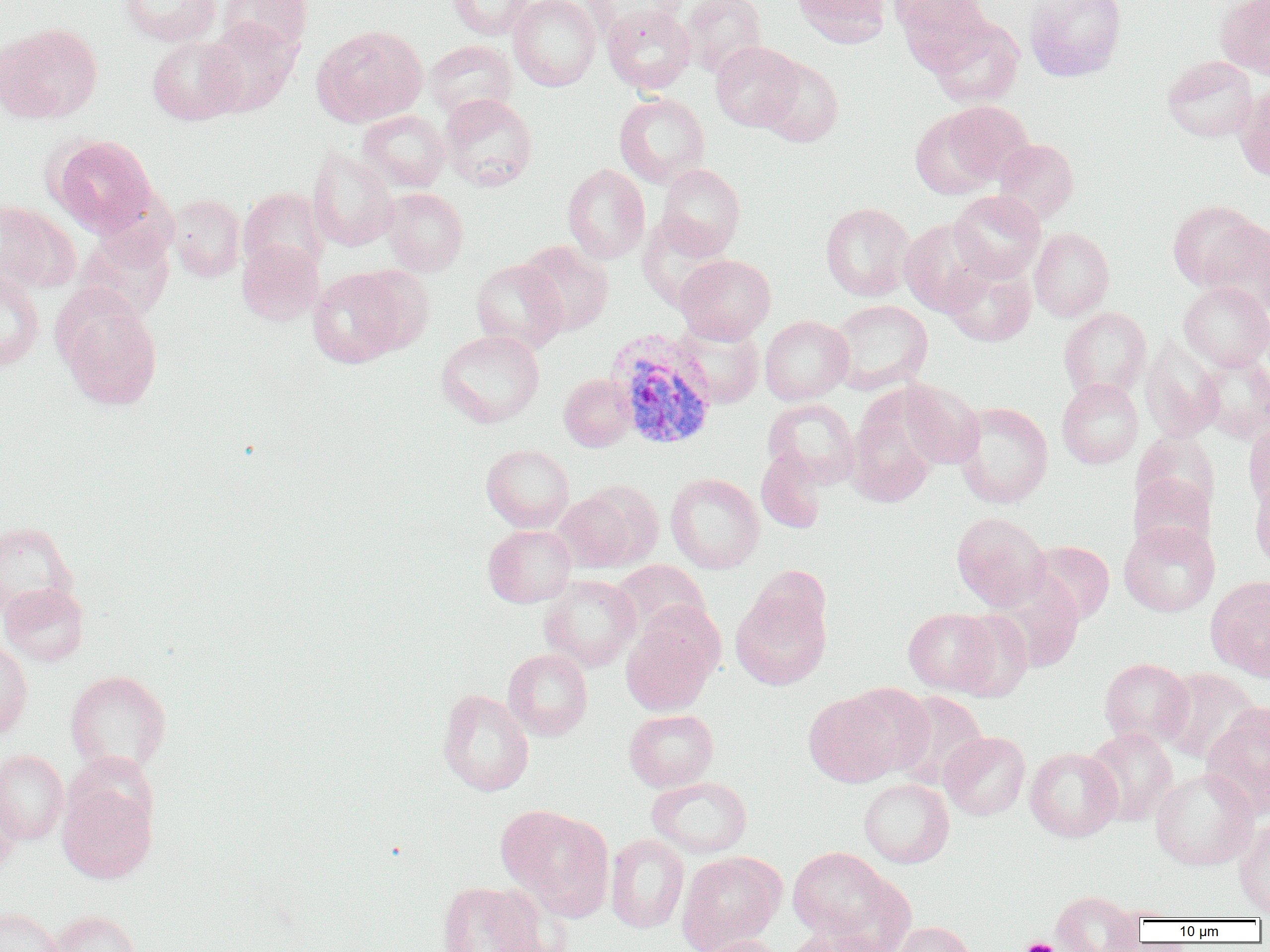 Approximate bounding boxes as [x1, y1, x2, y2] in pixels. Uninfected red blood cell locations: [119, 0, 221, 46], [218, 0, 312, 57], [447, 0, 534, 40], [509, 0, 600, 91], [583, 0, 688, 45], [680, 0, 767, 77], [792, 0, 890, 47], [893, 0, 991, 62], [1025, 0, 1126, 82], [1217, 0, 1270, 80], [602, 5, 696, 94], [927, 17, 1024, 108], [200, 18, 300, 117], [0, 23, 103, 123], [311, 24, 428, 127], [147, 36, 245, 125], [424, 40, 517, 119], [711, 41, 803, 131], [1162, 55, 1259, 142], [758, 58, 843, 147], [1234, 84, 1270, 183], [614, 92, 710, 187], [439, 93, 538, 191], [938, 100, 1034, 185], [910, 107, 1003, 200], [358, 110, 451, 192], [49, 135, 156, 235], [993, 138, 1079, 224], [308, 147, 399, 251], [656, 163, 745, 258], [562, 164, 650, 264], [238, 187, 328, 278], [381, 188, 468, 276], [948, 190, 1046, 282], [167, 194, 246, 282], [0, 200, 79, 294], [1167, 200, 1264, 291], [820, 203, 915, 301], [637, 214, 732, 312], [1200, 218, 1270, 319], [899, 219, 995, 315], [1029, 227, 1114, 321], [517, 240, 614, 335], [237, 241, 324, 326], [676, 254, 776, 344], [941, 258, 1037, 347], [471, 259, 568, 352], [0, 267, 45, 372], [308, 268, 410, 368], [1178, 281, 1270, 371], [59, 300, 162, 410], [830, 300, 933, 394], [1059, 307, 1152, 400], [760, 315, 853, 404], [671, 322, 764, 409], [437, 329, 544, 428], [1140, 336, 1224, 442], [1196, 352, 1270, 443], [559, 374, 636, 451], [1057, 378, 1143, 468], [897, 381, 984, 470], [845, 391, 943, 507], [763, 398, 860, 488], [954, 401, 1053, 508], [1243, 420, 1270, 509], [1130, 432, 1221, 521], [481, 444, 574, 532], [755, 447, 828, 534], [1129, 471, 1216, 557], [665, 473, 764, 573], [1249, 480, 1270, 572], [553, 486, 654, 573], [951, 512, 1051, 611], [0, 521, 78, 618], [1119, 521, 1220, 617], [483, 525, 576, 607], [1025, 541, 1115, 625], [611, 560, 710, 643], [986, 574, 1084, 673], [539, 575, 641, 672], [1206, 576, 1270, 681], [0, 582, 89, 666], [730, 585, 831, 690], [903, 608, 998, 695], [949, 610, 1033, 701], [621, 618, 719, 716], [0, 637, 33, 741], [503, 649, 593, 740], [1099, 658, 1194, 749], [1157, 668, 1261, 765], [65, 670, 172, 776], [841, 683, 933, 778], [437, 688, 534, 797], [803, 691, 905, 787], [889, 691, 989, 790], [1201, 704, 1270, 819], [624, 709, 719, 792], [1082, 728, 1178, 826], [939, 731, 1030, 820], [1025, 747, 1122, 842], [0, 749, 69, 844], [1150, 768, 1258, 870], [647, 777, 752, 858], [858, 779, 954, 868], [0, 783, 22, 874], [57, 784, 157, 882], [497, 804, 614, 920], [1234, 818, 1270, 917], [605, 833, 689, 934], [787, 847, 896, 944], [677, 851, 785, 952], [436, 881, 550, 952], [1050, 890, 1142, 952], [0, 907, 63, 952], [48, 910, 141, 952], [891, 921, 978, 952], [783, 927, 890, 952], [695, 935, 784, 952]. Plasmodium vivax-infected red blood cell locations: [605, 328, 719, 452]. Platelet locations: [1018, 938, 1061, 952]. Slide-level diagnosis: Plasmodium vivax. Thin blood film. Image is 1270×952 pixels. One field of a larger specimen. 1000x magnification. Optical microscopy.